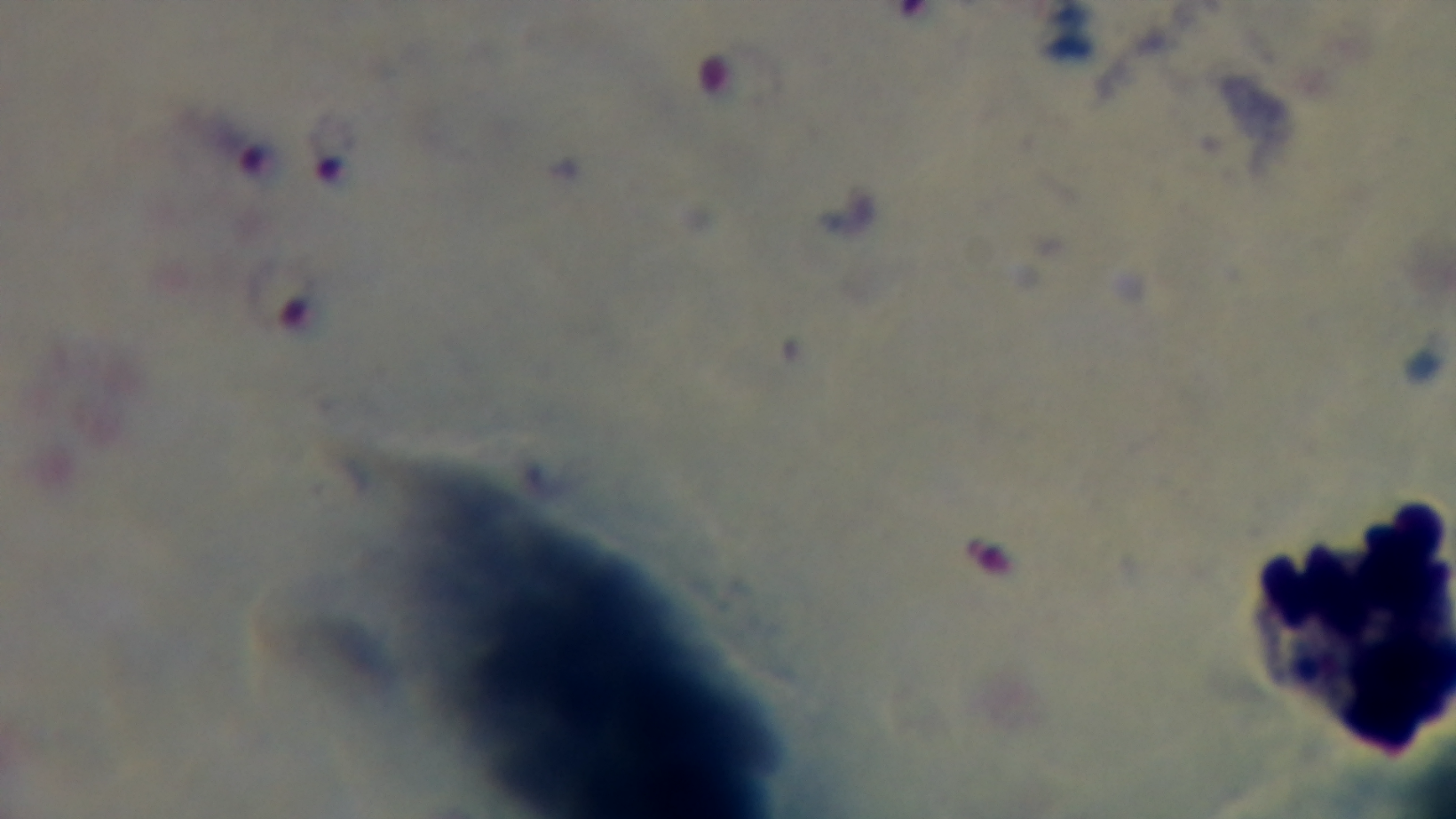

stain = Giemsa
malaria status = positive
field of view = one from the slide
capture = mounted 4K digital camera
preparation = thick smear
modality = light microscopy
objective = 100x oil immersion